Classify this cell by malaria status.
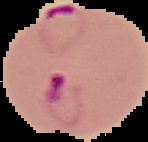

It is parasitized.

Summary:
  - Image size: 148×142 pixels
  - Image type: cell region segmented out of the field of view; surrounding area masked to black
  - Preparation: thin blood smear